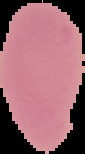
preparation = thin blood smear
result = no Plasmodium parasites seen
image size = 85×154 pixels
image type = cell region segmented out of the field of view; surrounding area masked to black